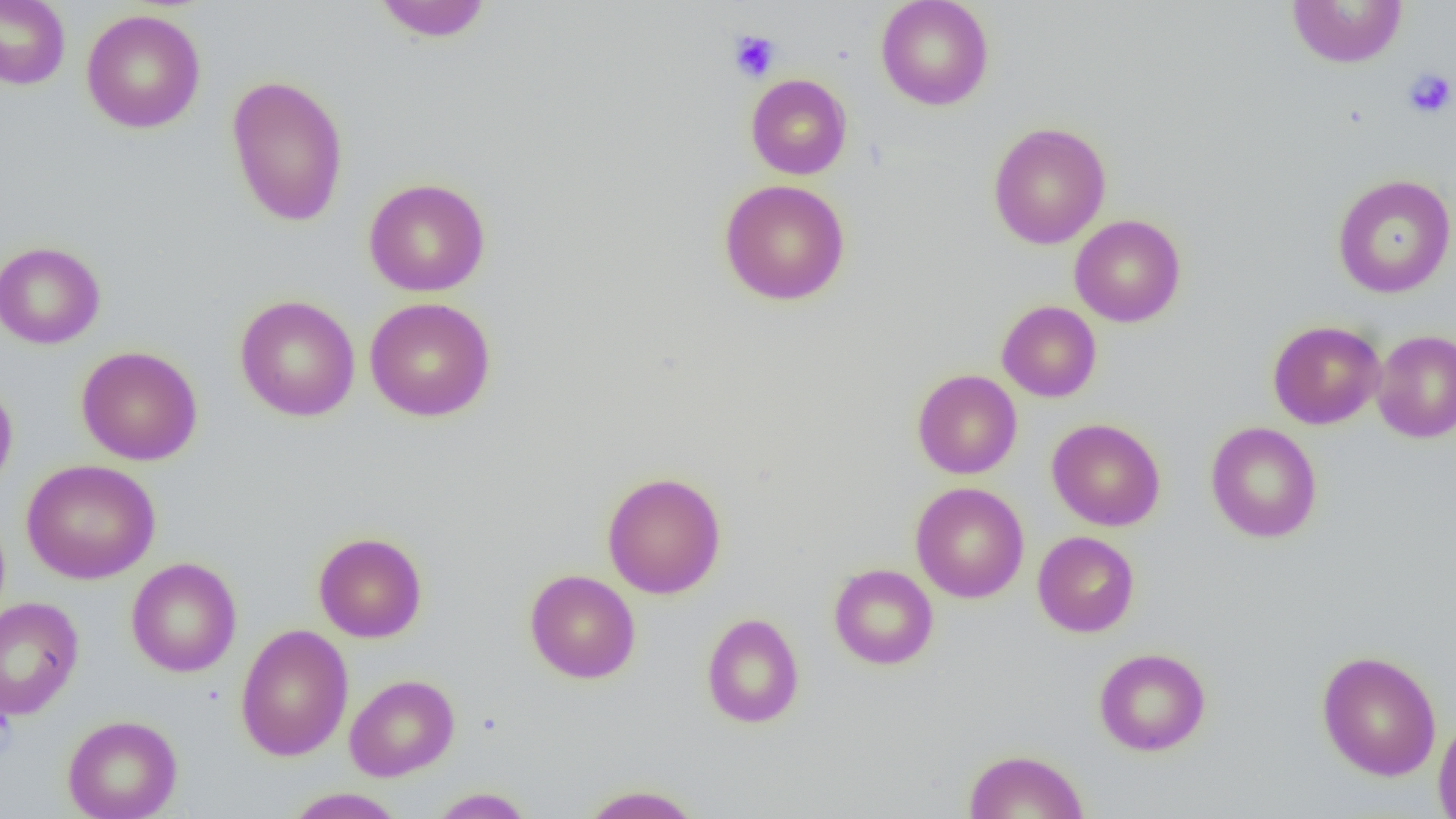
Approximate bounding boxes as [x1, y1, x2, y2] in pixels. Platelet locations: [729, 30, 781, 82], [1403, 68, 1455, 119]. Uninfected red blood cell locations: [0, 0, 71, 90], [371, 0, 494, 43], [876, 0, 994, 110], [1286, 1, 1408, 68], [81, 8, 206, 133], [745, 73, 852, 179], [226, 74, 348, 227], [988, 122, 1111, 249], [1332, 174, 1456, 298], [363, 177, 490, 297], [719, 179, 851, 306], [1069, 214, 1186, 327], [0, 241, 106, 349], [235, 294, 361, 422], [365, 297, 496, 422], [997, 300, 1102, 402], [1268, 320, 1385, 429], [1372, 329, 1456, 444], [77, 346, 203, 465], [912, 369, 1022, 479], [0, 376, 18, 495], [1047, 418, 1165, 531], [1205, 421, 1322, 543], [20, 459, 160, 584], [602, 470, 727, 599], [911, 482, 1029, 603], [1032, 531, 1139, 637], [314, 532, 428, 643], [125, 557, 241, 677], [828, 564, 939, 670], [525, 569, 640, 684], [0, 596, 85, 720], [701, 612, 804, 728], [235, 624, 354, 761], [1094, 647, 1211, 756], [1317, 650, 1442, 781], [345, 674, 460, 782], [62, 714, 182, 819], [1433, 715, 1456, 817], [963, 749, 1090, 819], [578, 784, 705, 818], [284, 787, 407, 819], [428, 787, 536, 818]. Slide-level diagnosis: negative for blood parasites. Thin blood smear. Image is 1456×819 pixels. Single field of view. Optical microscopy. Captured at 1000x magnification.